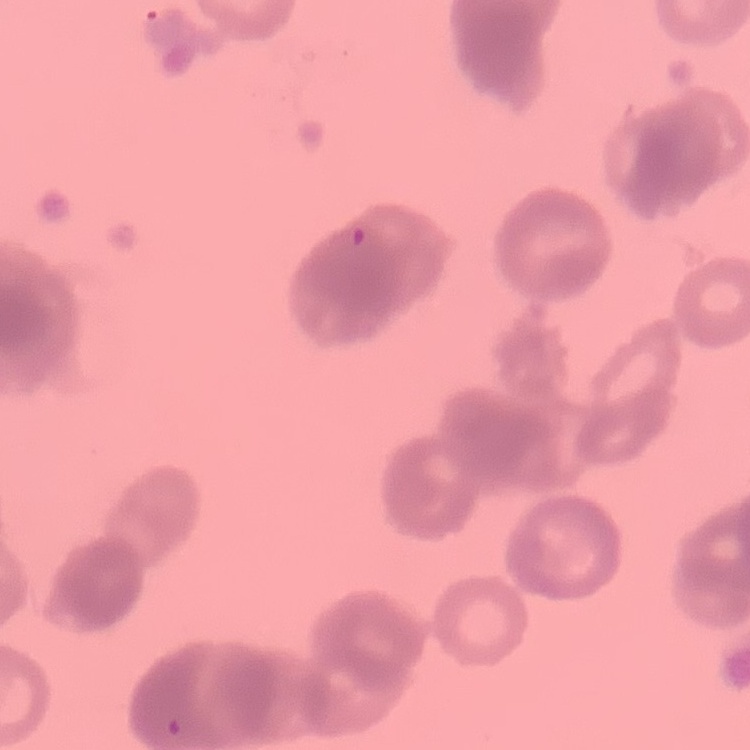
The red blood cells show rouleaux formation. Field's or Giemsa stain. Thin blood film. Square crop of a larger photomicrograph.